Give the preparation type.
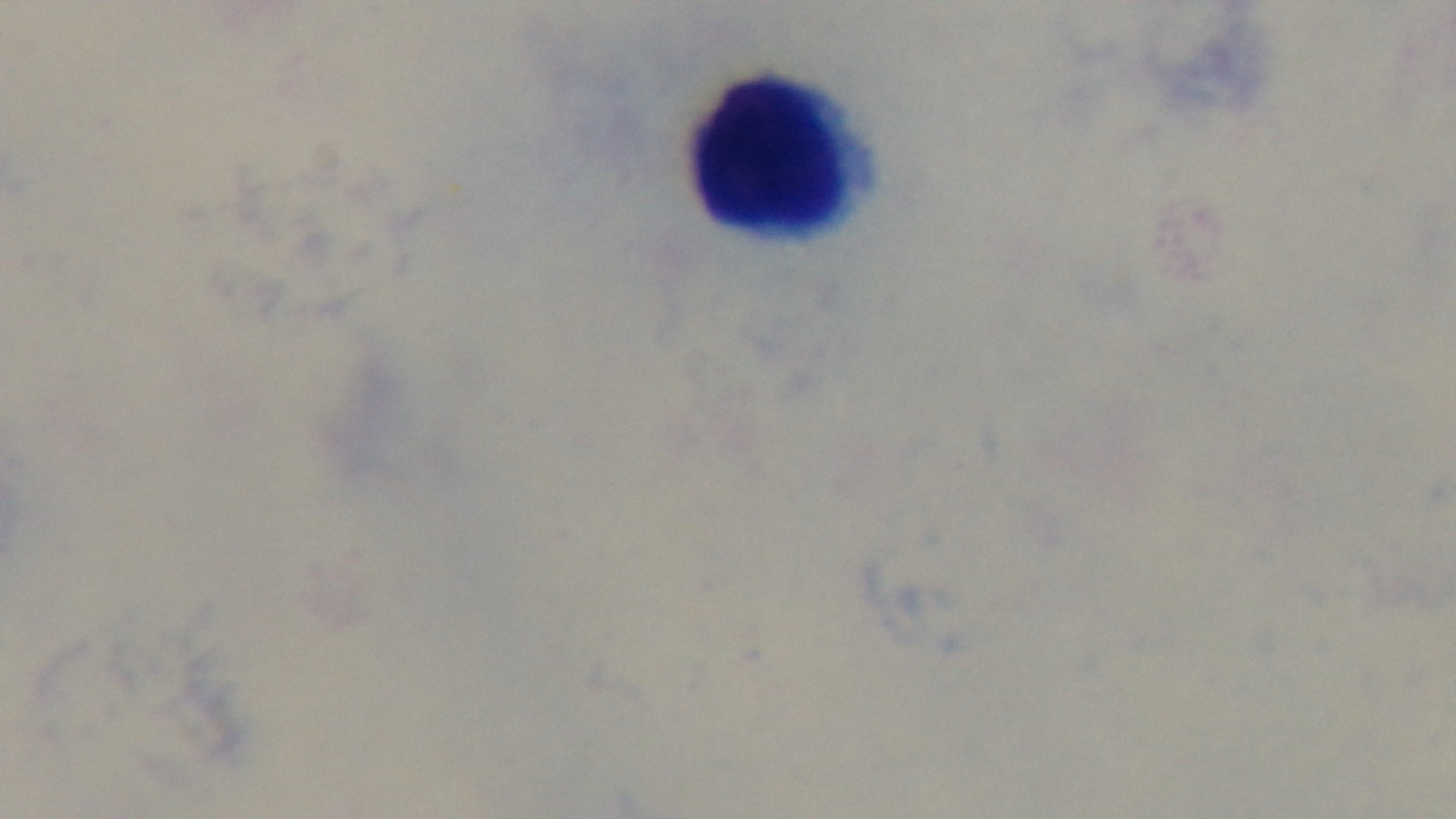
Thick.

malaria status = uninfected
field of view = one from the slide
objective = 100x oil immersion
capture = mounted 4K digital camera
modality = light microscopy
stain = Giemsa